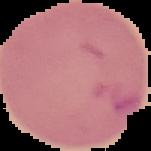

{
  "image_type": "segmented cell region on a black background",
  "preparation": "thin blood smear",
  "image_size": "151×151 pixels",
  "malaria_status": "parasitized"
}